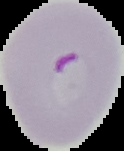

Summary:
  - Malaria status: parasitized
  - Image type: segmented cell region on a black background
  - Image size: 124×151 pixels
  - Preparation: thin blood smear